State the preparation type.
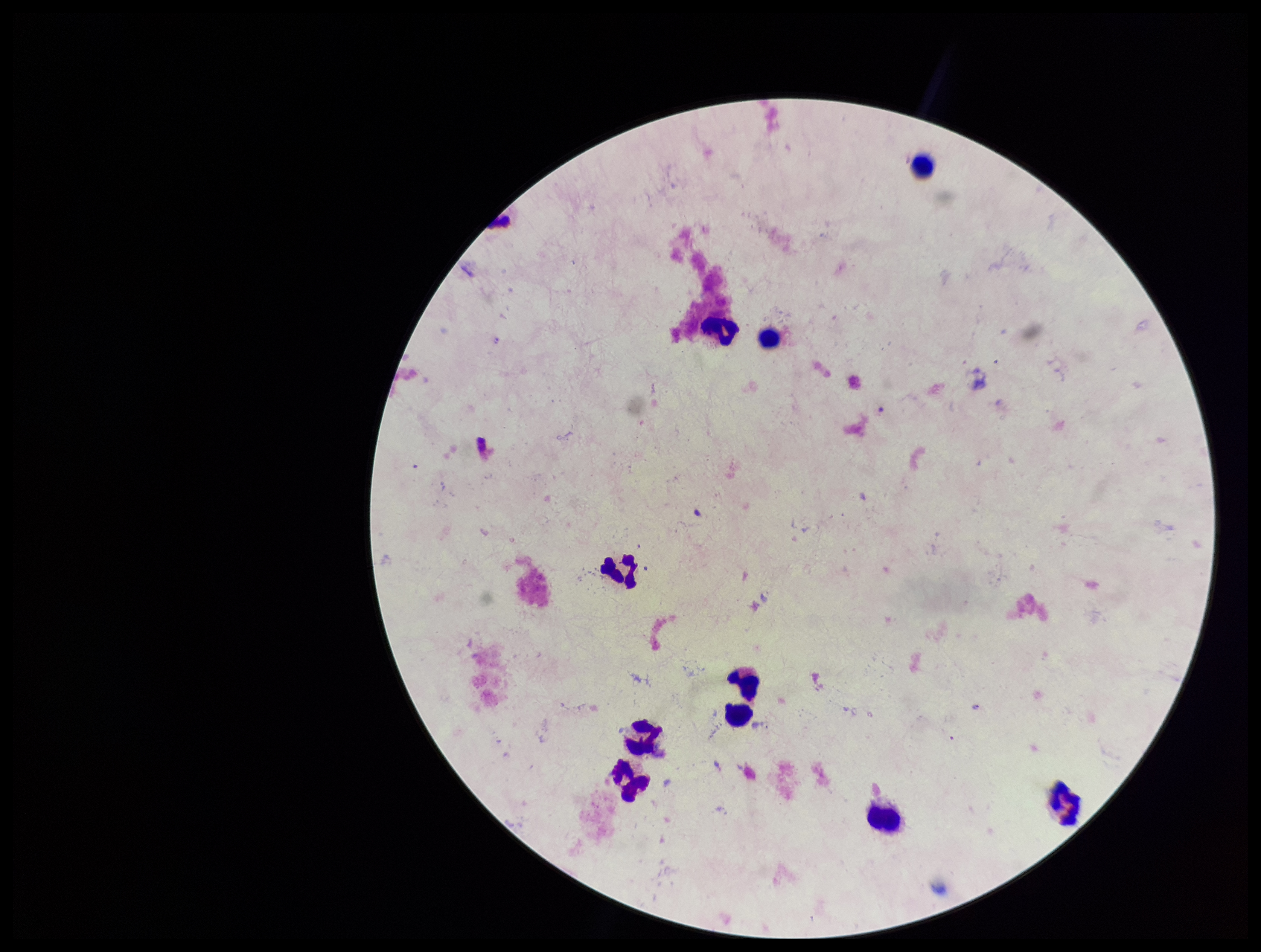
It is a thick blood smear.

{
  "image_size": "1261×952 pixels",
  "plasmodium_parasites": "none detected",
  "capture": "smartphone photograph through the microscope eyepiece",
  "stain": "Giemsa",
  "parasite_count": 0,
  "field_of_view": "one from this slide",
  "patient_malaria_status": "negative",
  "leukocyte_count": 10
}